Identify the parasite.
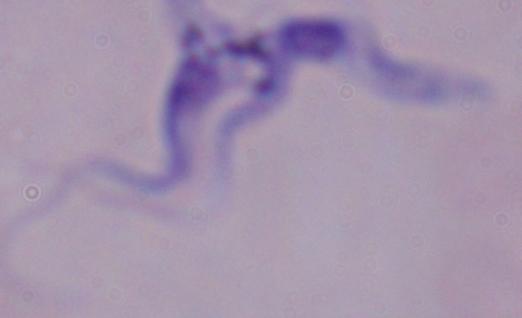
A trypanosome.

Summary:
  - Modality: photomicrograph
  - Magnification: 1000x